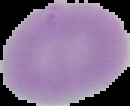

image_size: 130×106 pixels
preparation: thin blood smear
malaria_status: uninfected
image_type: segmented cell region with the area outside set to black